Comment on the morphology of the erythrocytes.
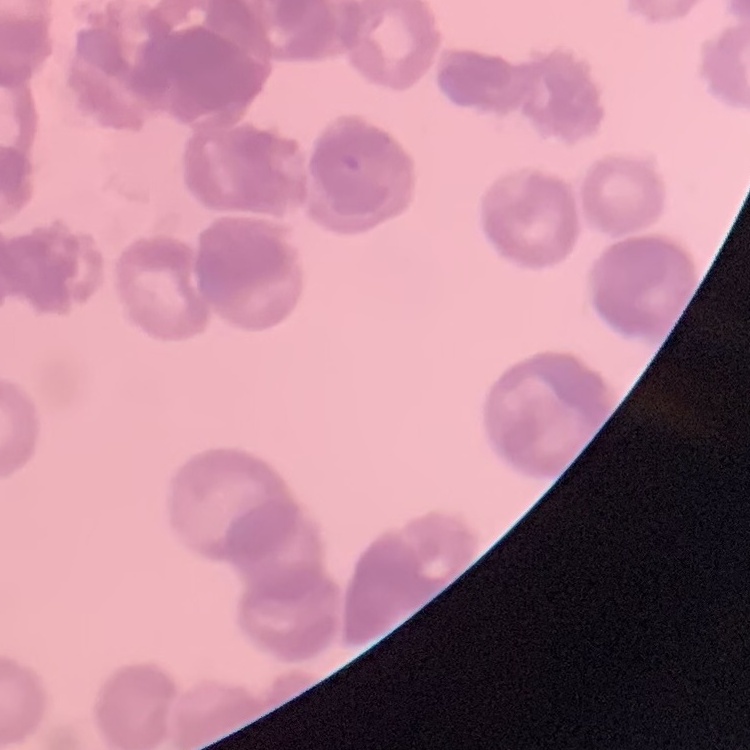
Rouleaux formation.

Thin peripheral smear. Stained with either Field's or Giemsa. Square crop of a larger photomicrograph.